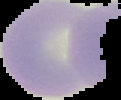
preparation = thin blood smear
malaria status = uninfected
image size = 121×100 pixels
image type = segmented cell region on a black background